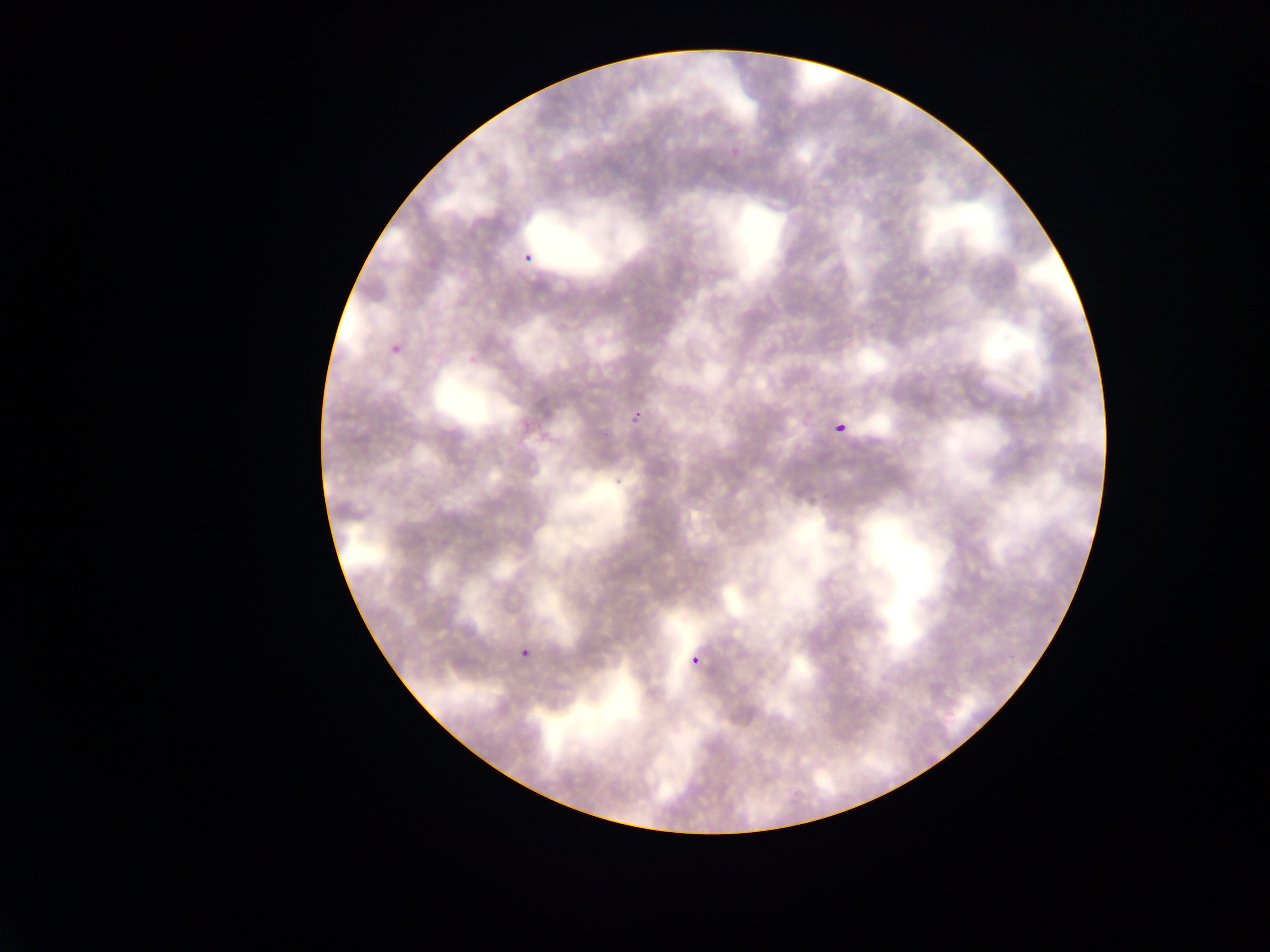

Approximate bounding boxes as [left, top, right, bottom] in pixels.
Summary:
  - Plasmodium parasite locations: [517, 242, 545, 261], [390, 331, 412, 349], [624, 405, 642, 428], [831, 418, 850, 437], [514, 638, 538, 661], [688, 641, 708, 663]
  - Preparation: thin blood film
  - Image size: 1270×952 pixels
  - Country: Ghana
  - Field of view: single
  - Capture: mobile-phone photograph through a microscope